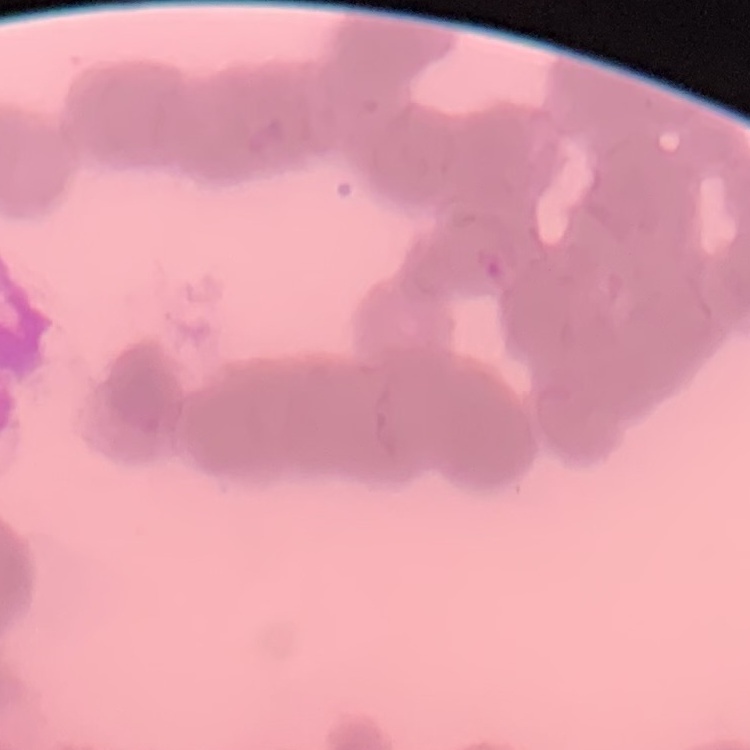
Summary:
  - Red blood cell morphology: rouleaux formation
  - Image type: square crop of a larger photomicrograph
  - Preparation: thin blood smear
  - Stain: Field's or Giemsa